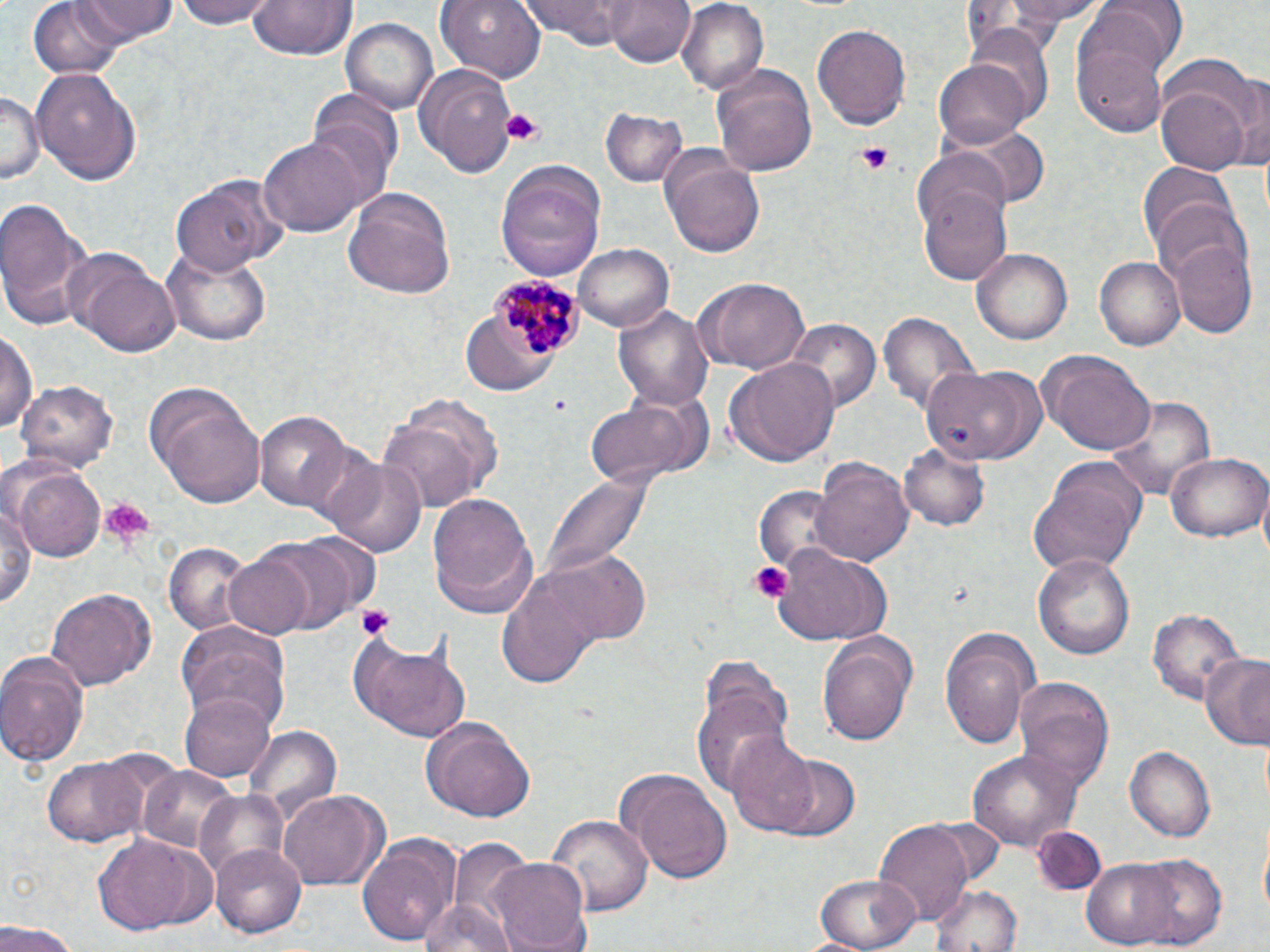
Summary:
  - Coordinate format: approximate bounding boxes as named x1/y1/x2/y2 corners in pixels
  - Platelet locations: (x1=496, y1=108, x2=546, y2=146), (x1=856, y1=143, x2=895, y2=175), (x1=549, y1=396, x2=567, y2=410), (x1=94, y1=497, x2=154, y2=552), (x1=749, y1=561, x2=790, y2=602), (x1=354, y1=604, x2=397, y2=642)
  - Plasmodium malariae-infected red blood cell locations: (x1=489, y1=275, x2=589, y2=362)
  - Uninfected red blood cell locations: (x1=71, y1=0, x2=177, y2=45), (x1=174, y1=0, x2=279, y2=30), (x1=249, y1=0, x2=356, y2=62), (x1=436, y1=0, x2=545, y2=83), (x1=519, y1=0, x2=633, y2=49), (x1=607, y1=0, x2=695, y2=67), (x1=675, y1=0, x2=768, y2=93), (x1=972, y1=0, x2=1108, y2=45), (x1=993, y1=0, x2=1113, y2=25), (x1=29, y1=1, x2=126, y2=79), (x1=1084, y1=1, x2=1189, y2=74), (x1=341, y1=16, x2=439, y2=115), (x1=1072, y1=18, x2=1173, y2=137), (x1=812, y1=22, x2=913, y2=130), (x1=933, y1=58, x2=1033, y2=149), (x1=415, y1=62, x2=515, y2=175), (x1=711, y1=63, x2=818, y2=177), (x1=33, y1=64, x2=143, y2=185), (x1=1230, y1=74, x2=1270, y2=173), (x1=1157, y1=85, x2=1253, y2=173), (x1=1, y1=89, x2=39, y2=187), (x1=310, y1=89, x2=403, y2=199), (x1=601, y1=107, x2=688, y2=189), (x1=957, y1=122, x2=1048, y2=207), (x1=258, y1=136, x2=368, y2=240), (x1=660, y1=148, x2=767, y2=257), (x1=494, y1=161, x2=607, y2=281), (x1=1138, y1=162, x2=1235, y2=255), (x1=171, y1=176, x2=279, y2=276), (x1=918, y1=179, x2=1011, y2=286), (x1=343, y1=187, x2=457, y2=299), (x1=0, y1=198, x2=95, y2=331), (x1=1152, y1=199, x2=1251, y2=290), (x1=1170, y1=238, x2=1259, y2=339), (x1=576, y1=242, x2=674, y2=330), (x1=63, y1=247, x2=181, y2=357), (x1=163, y1=248, x2=273, y2=347), (x1=972, y1=249, x2=1071, y2=345), (x1=1095, y1=257, x2=1185, y2=350), (x1=700, y1=277, x2=810, y2=374), (x1=616, y1=302, x2=716, y2=414), (x1=877, y1=312, x2=980, y2=418), (x1=785, y1=316, x2=881, y2=412), (x1=2, y1=326, x2=38, y2=437), (x1=460, y1=334, x2=532, y2=395), (x1=1038, y1=351, x2=1155, y2=453), (x1=722, y1=358, x2=842, y2=469), (x1=924, y1=366, x2=1046, y2=467), (x1=18, y1=380, x2=117, y2=473), (x1=147, y1=389, x2=267, y2=507), (x1=1107, y1=394, x2=1217, y2=501), (x1=581, y1=396, x2=700, y2=489), (x1=379, y1=406, x2=497, y2=512), (x1=258, y1=411, x2=356, y2=515), (x1=898, y1=443, x2=991, y2=532), (x1=1166, y1=451, x2=1269, y2=543), (x1=319, y1=453, x2=428, y2=559), (x1=812, y1=458, x2=914, y2=568), (x1=1025, y1=458, x2=1147, y2=579), (x1=10, y1=463, x2=106, y2=562), (x1=542, y1=472, x2=652, y2=584), (x1=1, y1=489, x2=37, y2=619), (x1=753, y1=489, x2=834, y2=575), (x1=428, y1=491, x2=541, y2=617), (x1=253, y1=535, x2=364, y2=636), (x1=164, y1=545, x2=252, y2=634), (x1=770, y1=545, x2=891, y2=647), (x1=532, y1=549, x2=655, y2=646), (x1=1033, y1=552, x2=1135, y2=659), (x1=222, y1=554, x2=318, y2=639), (x1=492, y1=564, x2=611, y2=691), (x1=46, y1=587, x2=156, y2=691), (x1=1150, y1=607, x2=1246, y2=707), (x1=176, y1=623, x2=292, y2=730), (x1=939, y1=626, x2=1041, y2=749), (x1=352, y1=630, x2=471, y2=740), (x1=818, y1=636, x2=915, y2=750), (x1=0, y1=652, x2=88, y2=768), (x1=1201, y1=656, x2=1270, y2=751), (x1=1013, y1=676, x2=1115, y2=793), (x1=691, y1=683, x2=791, y2=799), (x1=181, y1=690, x2=277, y2=784), (x1=423, y1=718, x2=535, y2=825), (x1=245, y1=727, x2=339, y2=821), (x1=724, y1=733, x2=820, y2=837), (x1=1123, y1=745, x2=1215, y2=841), (x1=967, y1=748, x2=1082, y2=855), (x1=41, y1=752, x2=154, y2=848), (x1=773, y1=755, x2=860, y2=843), (x1=137, y1=765, x2=238, y2=856), (x1=624, y1=770, x2=734, y2=883), (x1=192, y1=789, x2=291, y2=883), (x1=280, y1=792, x2=387, y2=889), (x1=546, y1=812, x2=651, y2=919), (x1=874, y1=820, x2=975, y2=922), (x1=1034, y1=824, x2=1105, y2=892), (x1=358, y1=830, x2=461, y2=947), (x1=91, y1=831, x2=217, y2=937), (x1=210, y1=842, x2=308, y2=939), (x1=1129, y1=853, x2=1227, y2=951), (x1=487, y1=858, x2=594, y2=952), (x1=1079, y1=862, x2=1184, y2=946), (x1=814, y1=873, x2=921, y2=949), (x1=929, y1=880, x2=1024, y2=952), (x1=418, y1=899, x2=514, y2=952), (x1=0, y1=924, x2=79, y2=952)
  - Slide-level diagnosis: Plasmodium malariae
  - Magnification: 1000x
  - Image size: 1270×952 pixels
  - Field of view: single
  - Modality: optical microscopy
  - Stain: May-Grünwald-Giemsa
  - Preparation: thin blood smear